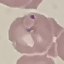
Summary:
  - Malaria status: parasitized
  - Capture: smartphone camera at the microscope eyepiece
  - Image type: automatically extracted cell patch, resized to 64 × 64 pixels
  - Preparation: thin blood film
  - Stain: Giemsa